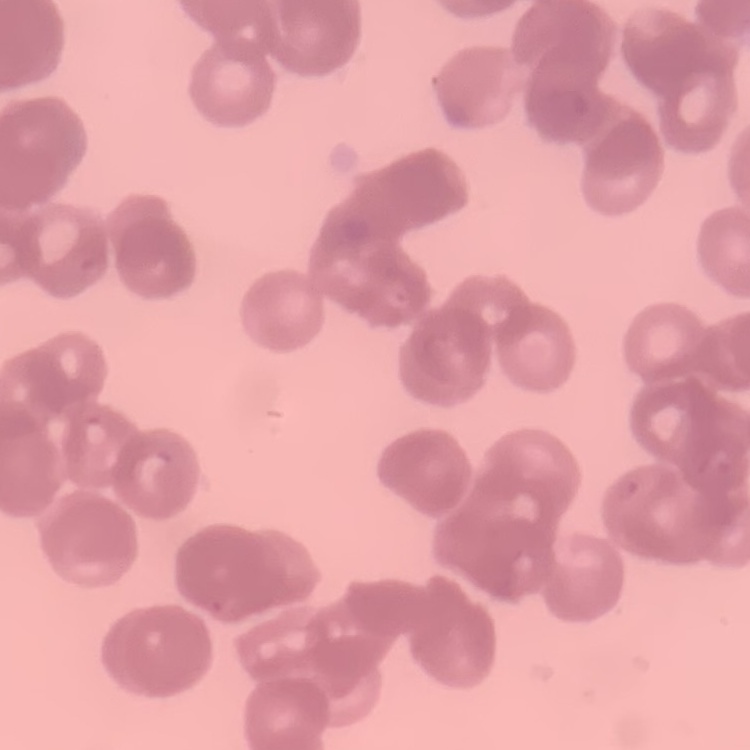

erythrocyte morphology = rouleaux formation
preparation = thin blood film
stain = Field's or Giemsa
image type = one tile cut from a larger photomicrograph